Classify this cell by malaria status.
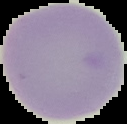

It is uninfected.

Segmented cell region on a black background. From a thin blood smear. Image is 127×124 pixels.